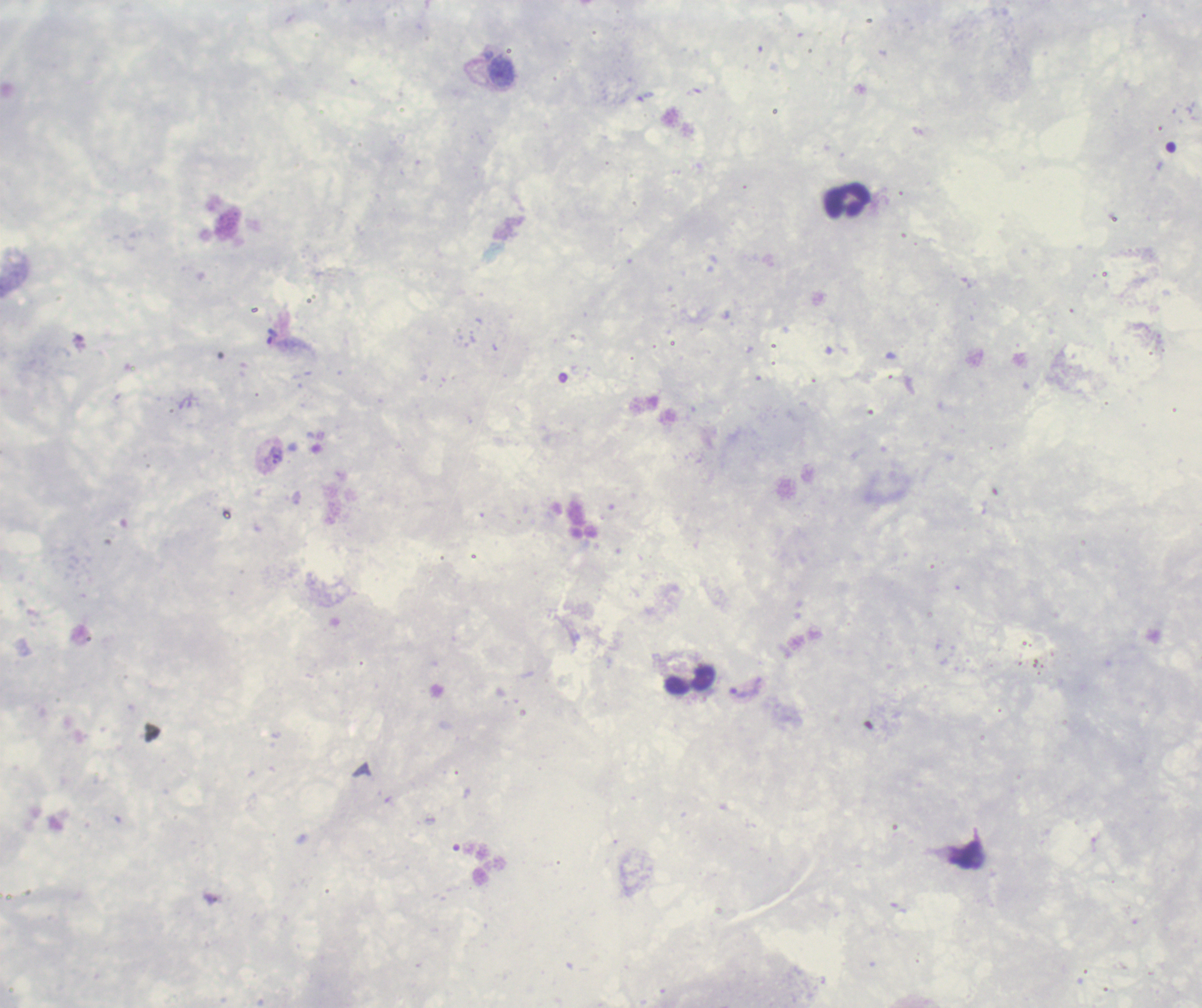

Approximate object centers, in pixels from the top-left corner.
Summary:
  - Leukocyte locations: (x=847, y=201), (x=691, y=681)
  - Trophozoite locations: (x=273, y=337), (x=744, y=691)
  - Context: previously used in an actual diagnosis
  - Image size: 1202×1008 pixels
  - Preparation: thick blood smear
  - Background quality: unsatisfactory
  - Result: Plasmodium parasites identified
  - Magnification: 100x
  - Field of view: one from this slide
  - Stain: Romanowsky